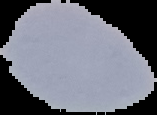 Malaria status: uninfected. Image is 157×115 pixels. The area outside the segmented cell region is set to black. From a thin blood film.